Locate every Babesia divergens-infected red blood cell.
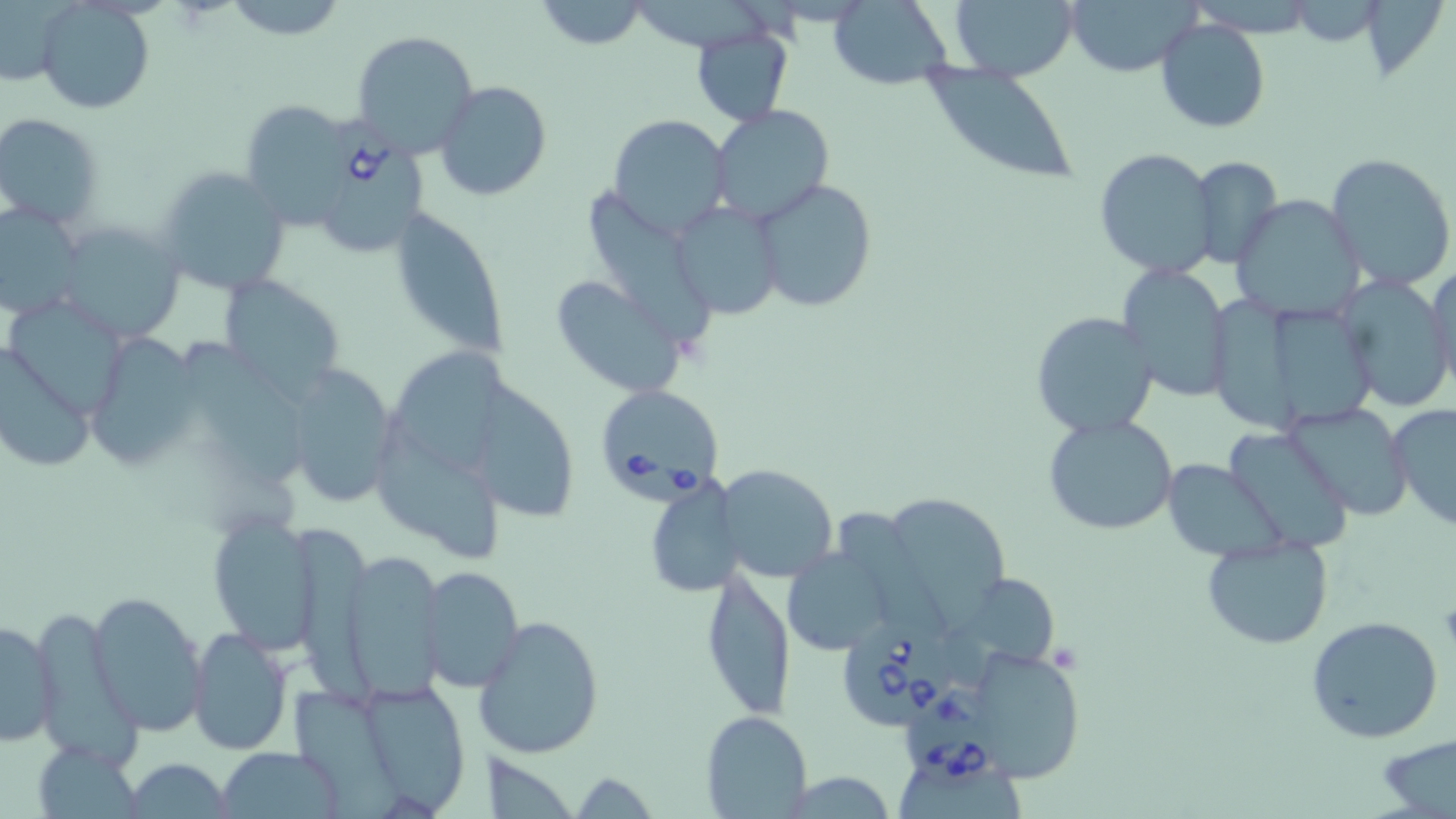

Approximate bounding boxes as named x1/y1/x2/y2 corners in pixels.
Babesia divergens-infected red blood cells: (x1=309, y1=140, x2=428, y2=257), (x1=596, y1=384, x2=724, y2=495), (x1=843, y1=613, x2=952, y2=733), (x1=905, y1=683, x2=1002, y2=795).

Uninfected red blood cell locations: (x1=219, y1=0, x2=349, y2=40), (x1=533, y1=0, x2=651, y2=51), (x1=950, y1=0, x2=1078, y2=81), (x1=1064, y1=0, x2=1200, y2=77), (x1=37, y1=1, x2=154, y2=114), (x1=827, y1=1, x2=952, y2=88), (x1=1156, y1=16, x2=1270, y2=133), (x1=689, y1=26, x2=794, y2=125), (x1=352, y1=30, x2=479, y2=158), (x1=918, y1=64, x2=1085, y2=188), (x1=435, y1=80, x2=554, y2=201), (x1=240, y1=100, x2=357, y2=226), (x1=711, y1=103, x2=834, y2=223), (x1=0, y1=112, x2=105, y2=228), (x1=610, y1=113, x2=732, y2=236), (x1=1094, y1=148, x2=1220, y2=280), (x1=1326, y1=153, x2=1456, y2=290), (x1=1189, y1=156, x2=1283, y2=269), (x1=155, y1=165, x2=292, y2=296), (x1=755, y1=179, x2=878, y2=310), (x1=587, y1=193, x2=713, y2=347), (x1=1232, y1=196, x2=1365, y2=323), (x1=670, y1=198, x2=784, y2=319), (x1=0, y1=201, x2=86, y2=321), (x1=389, y1=208, x2=510, y2=359), (x1=55, y1=222, x2=185, y2=343), (x1=1426, y1=260, x2=1456, y2=395), (x1=1117, y1=262, x2=1232, y2=402), (x1=551, y1=272, x2=690, y2=398), (x1=1335, y1=273, x2=1453, y2=413), (x1=220, y1=274, x2=345, y2=401), (x1=1209, y1=292, x2=1303, y2=437), (x1=9, y1=297, x2=122, y2=414), (x1=1280, y1=306, x2=1377, y2=431), (x1=1030, y1=313, x2=1155, y2=436), (x1=88, y1=331, x2=199, y2=469), (x1=190, y1=335, x2=313, y2=487), (x1=0, y1=340, x2=95, y2=474), (x1=390, y1=348, x2=515, y2=483), (x1=282, y1=362, x2=400, y2=510), (x1=484, y1=386, x2=577, y2=527), (x1=1285, y1=401, x2=1411, y2=521), (x1=1387, y1=402, x2=1456, y2=531), (x1=1043, y1=414, x2=1179, y2=536), (x1=1223, y1=426, x2=1354, y2=553), (x1=367, y1=438, x2=503, y2=564), (x1=1162, y1=458, x2=1283, y2=562), (x1=714, y1=464, x2=837, y2=583), (x1=644, y1=478, x2=743, y2=594), (x1=893, y1=489, x2=1008, y2=631), (x1=207, y1=511, x2=320, y2=655), (x1=301, y1=525, x2=386, y2=708), (x1=1198, y1=535, x2=1336, y2=651), (x1=782, y1=543, x2=896, y2=654), (x1=331, y1=546, x2=448, y2=702), (x1=421, y1=564, x2=524, y2=691), (x1=700, y1=564, x2=797, y2=720), (x1=87, y1=592, x2=208, y2=734), (x1=33, y1=606, x2=138, y2=773), (x1=474, y1=613, x2=606, y2=759), (x1=1, y1=615, x2=60, y2=749), (x1=1305, y1=615, x2=1443, y2=743), (x1=187, y1=624, x2=295, y2=756), (x1=970, y1=642, x2=1085, y2=781), (x1=370, y1=685, x2=466, y2=811), (x1=291, y1=689, x2=407, y2=818), (x1=700, y1=710, x2=813, y2=818), (x1=1382, y1=736, x2=1456, y2=816), (x1=217, y1=746, x2=342, y2=818), (x1=121, y1=759, x2=236, y2=818), (x1=568, y1=770, x2=659, y2=818), (x1=780, y1=772, x2=900, y2=817). Slide-level diagnosis: Babesia divergens. May-Grünwald-Giemsa-stained preparation. 1000x magnification. Image is 1456×819 pixels. Thin blood film. One field of a larger specimen. Optical microscopy.